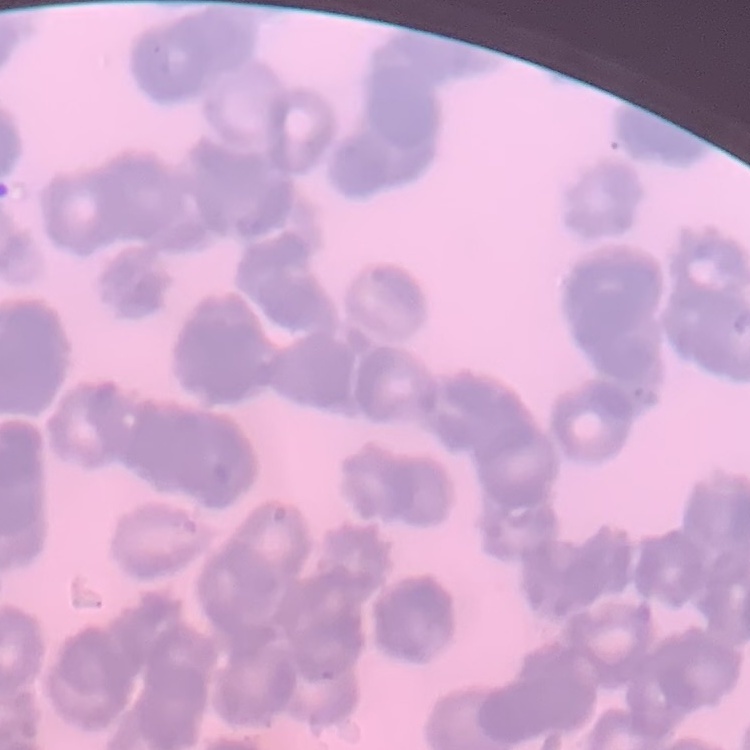

The erythrocytes exhibit rouleaux formation. Thin blood film. One tile cut from a larger photomicrograph. Field's or Giemsa stain.